Assess the morphology of the red blood cells.
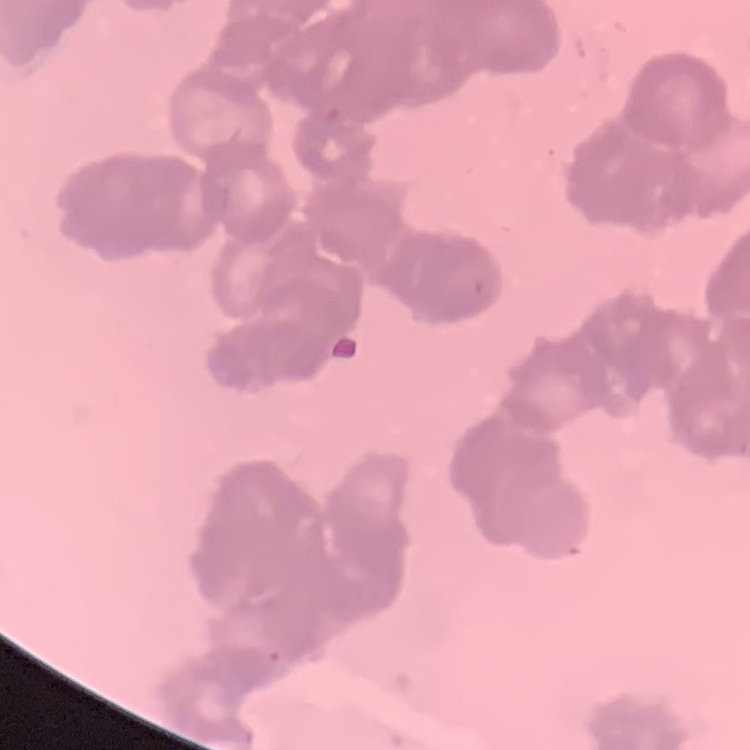

Rouleaux formation.

image_type: one tile cut from a larger photomicrograph
preparation: thin blood film
stain: Field's or Giemsa